State which parasite is depicted.
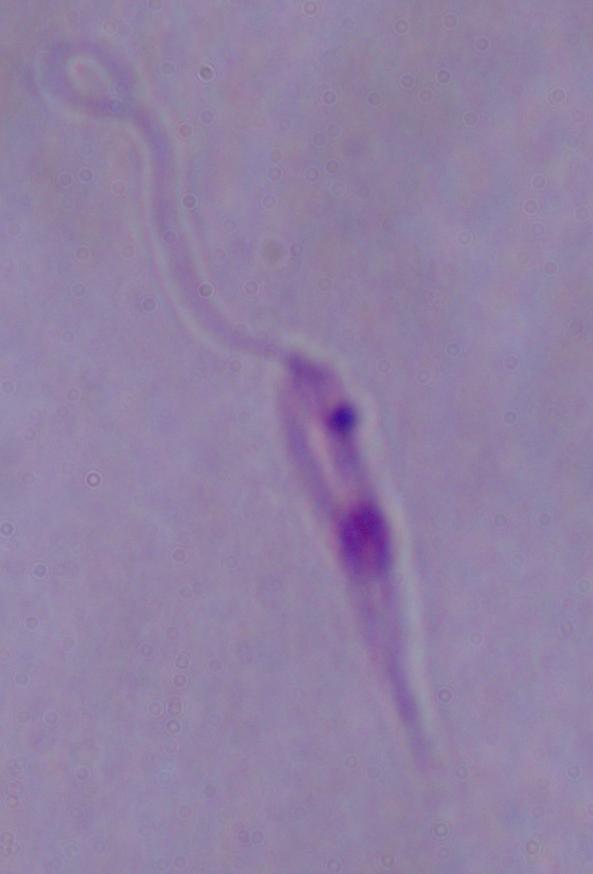
Leishmania.

{
  "modality": "micrograph",
  "magnification": "1000x"
}